Assess this cell for malaria.
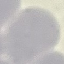
It is uninfected.

Summary:
  - Stain: Giemsa
  - Capture: smartphone through the microscope eyepiece
  - Preparation: thin blood film
  - Image type: automatically extracted cell patch, resized to 64 × 64 pixels